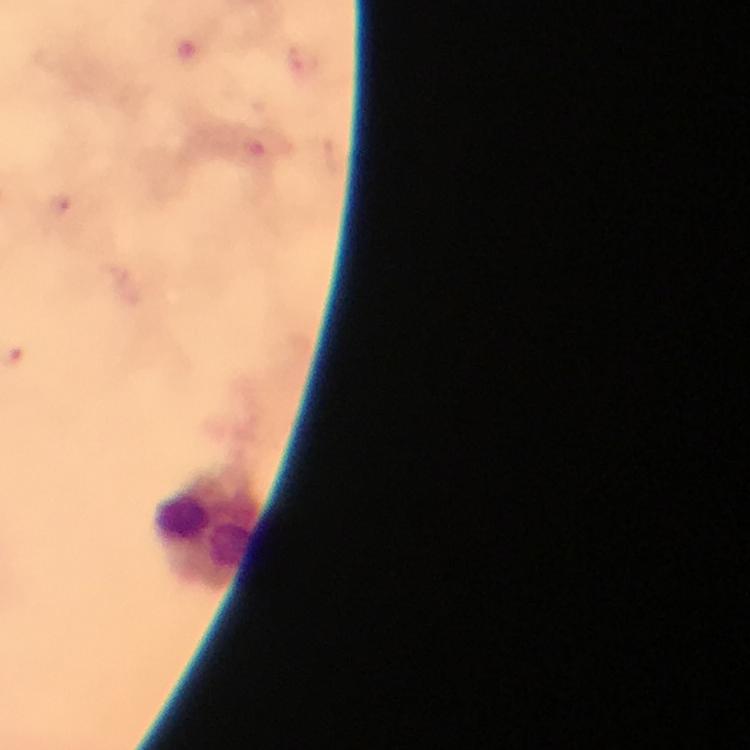

{
  "image_size": "750×750 pixels",
  "cropped_from": "a single field of view",
  "context": "from a diagnostic examination for malaria",
  "capture": "smartphone mounted on the microscope",
  "stain": "Giemsa",
  "leukocyte_locations": "approximate centers as (x, y) in pixels: (205, 532)",
  "malaria_parasites": "none detected",
  "magnification": "100x",
  "immersion_oil": "applied",
  "preparation": "thick smear"
}